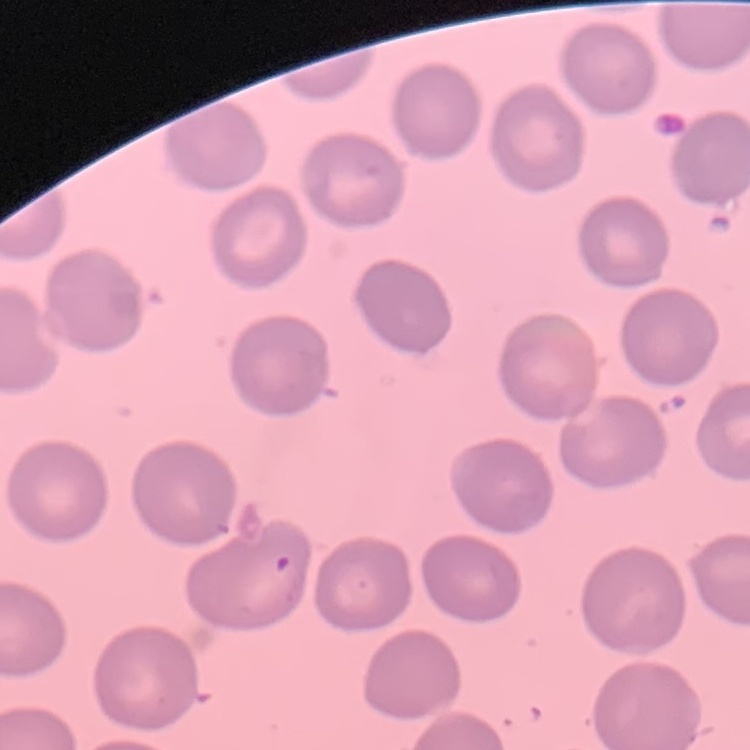
The red blood cells exhibit no rouleaux formation. Field's or Giemsa stain. Thin blood smear. One tile cut from a larger photomicrograph.